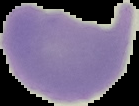
Summary:
  - Image type: segmented cell region on a black background
  - Result: no Plasmodium parasites seen
  - Preparation: thin blood film
  - Image size: 139×106 pixels